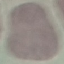

result = no malaria parasites seen
capture = smartphone camera at the microscope eyepiece
image type = automatically extracted cell patch, resized to 64 × 64 pixels
stain = Giemsa
preparation = thin smear